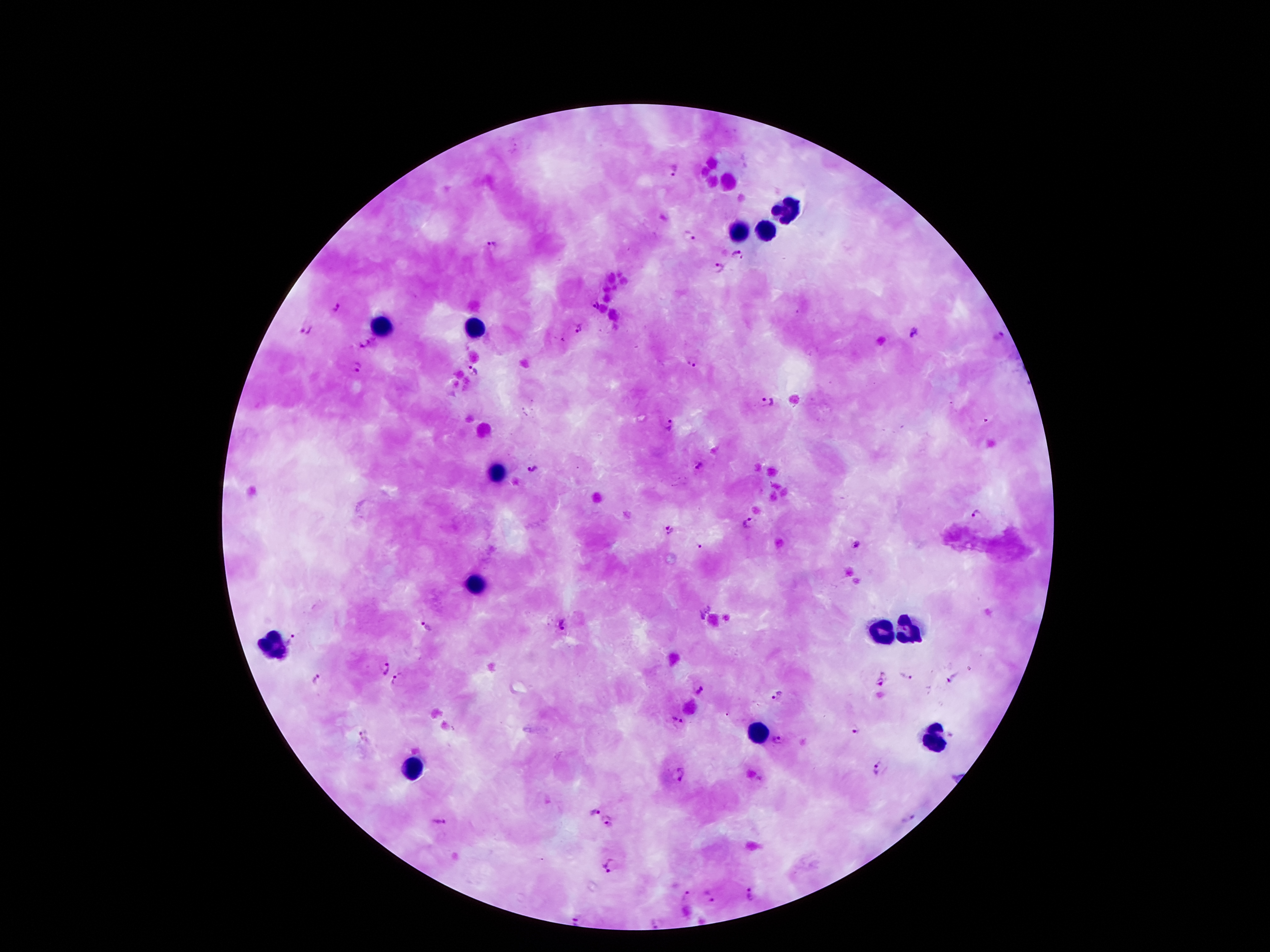

{
  "preparation": "thick blood smear",
  "stain": "Giemsa",
  "patient_malaria_status": "infected with Plasmodium falciparum",
  "magnification": "100x",
  "plasmodium_parasite_locations": "approximate object centers, in pixels from the top-left corner: (x=674, y=172), (x=688, y=237), (x=492, y=245), (x=737, y=255), (x=718, y=268), (x=336, y=310), (x=577, y=326), (x=304, y=330), (x=915, y=333), (x=364, y=344), (x=691, y=361), (x=356, y=369), (x=472, y=371), (x=765, y=401), (x=668, y=425), (x=697, y=466), (x=533, y=469), (x=977, y=513), (x=751, y=524), (x=669, y=528), (x=855, y=546), (x=698, y=547), (x=704, y=611), (x=563, y=625), (x=426, y=628), (x=293, y=638), (x=384, y=667), (x=905, y=676), (x=317, y=679), (x=397, y=679), (x=953, y=679), (x=879, y=680), (x=701, y=690), (x=776, y=696), (x=678, y=721), (x=856, y=733), (x=362, y=735), (x=777, y=740), (x=877, y=768), (x=680, y=773), (x=754, y=777), (x=593, y=810), (x=911, y=818), (x=610, y=820), (x=440, y=823), (x=609, y=865), (x=753, y=894), (x=687, y=897), (x=708, y=897), (x=581, y=919), (x=659, y=921)",
  "leukocyte_locations": "approximate object centers, in pixels from the top-left corner: (x=785, y=209), (x=736, y=230), (x=764, y=233), (x=380, y=327), (x=473, y=330), (x=496, y=470), (x=475, y=584), (x=908, y=625), (x=880, y=635), (x=272, y=648), (x=759, y=732), (x=936, y=739), (x=410, y=767)",
  "field_of_view": "one from this slide",
  "capture": "smartphone through the microscope eyepiece",
  "image_size": "1270×952 pixels"
}